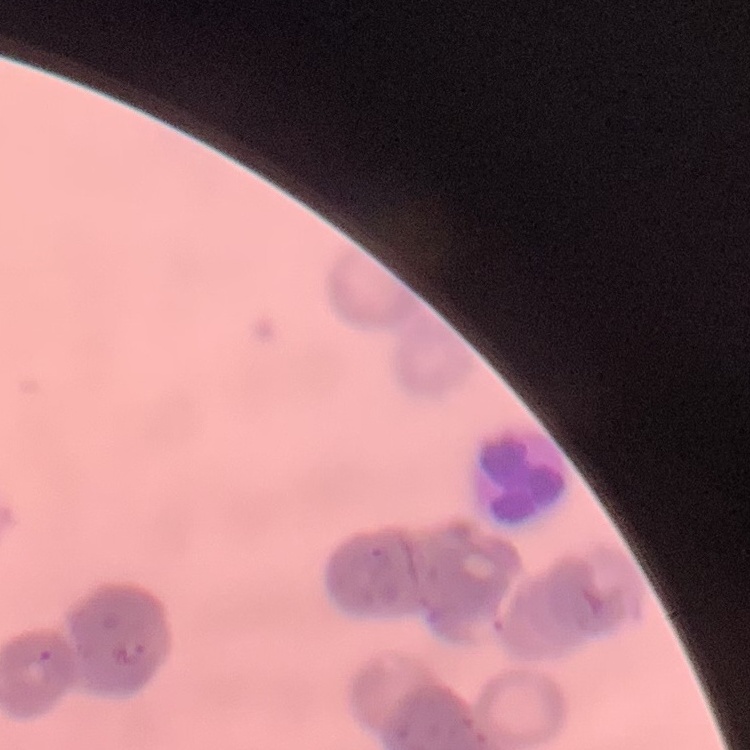

Summary:
  - Erythrocyte morphology: rouleaux formation
  - Stain: Field's or Giemsa
  - Image type: one tile cut from a larger photomicrograph
  - Preparation: thin peripheral smear